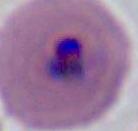 Photomicrograph. 400x or 1000x magnification. A Plasmodium parasite is shown.